Give the position of every Plasmodium parasite visible.
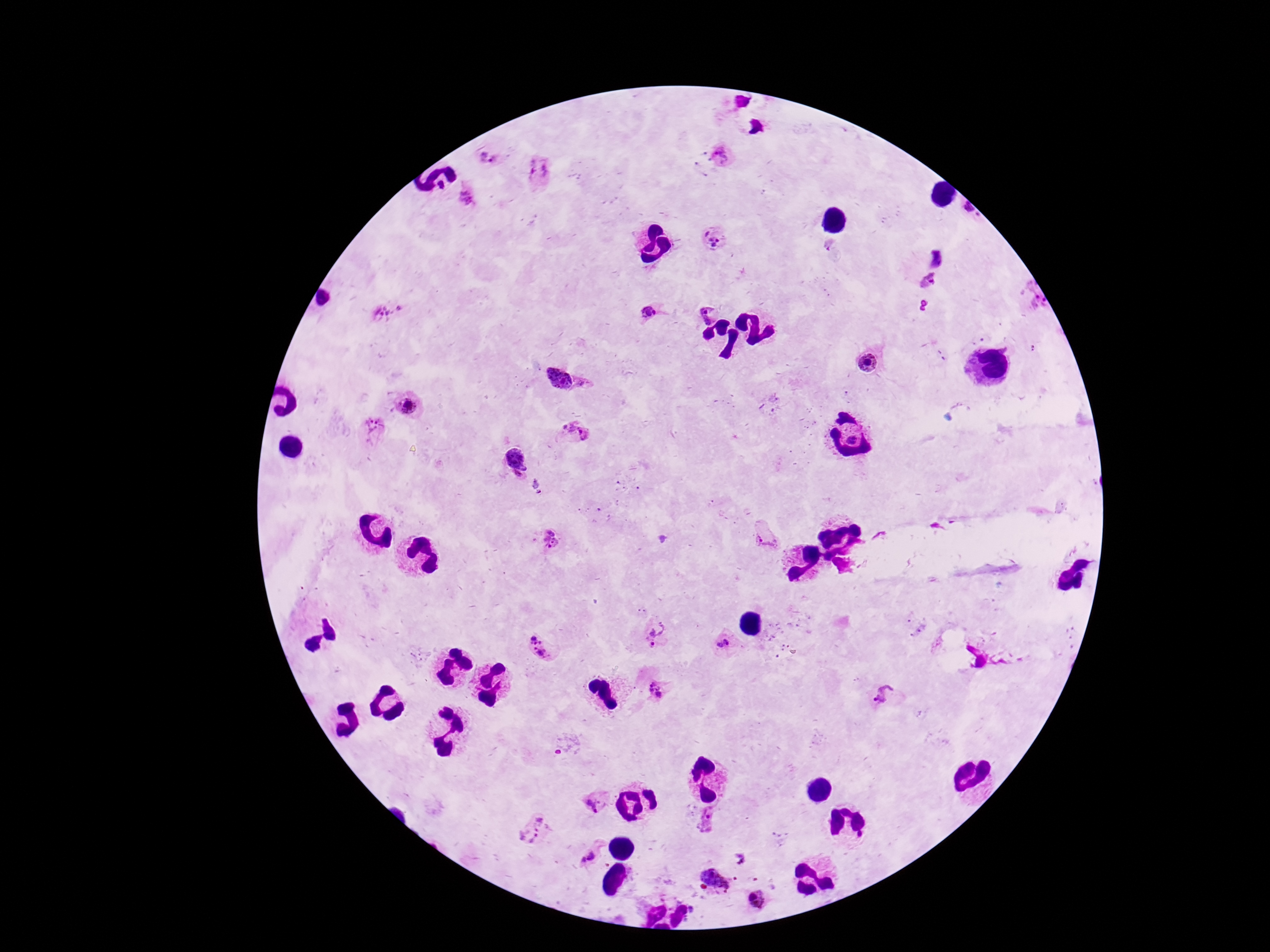
Approximate centers as {x, y} in pixels.
Plasmodium parasites: {489, 156}, {719, 158}, {537, 172}, {465, 196}, {713, 238}, {936, 256}, {929, 282}, {1028, 297}, {706, 311}, {387, 312}, {647, 314}, {868, 363}, {558, 377}, {584, 386}, {409, 404}, {372, 430}, {572, 432}, {514, 458}, {765, 536}, {551, 539}, {655, 633}, {724, 644}, {540, 648}, {658, 690}, {883, 695}, {597, 802}, {707, 818}, {533, 830}, {592, 855}, {719, 876}, {757, 900}.

{
  "preparation": "thick peripheral-blood smear",
  "magnification": "100x",
  "capture": "smartphone camera through the microscope eyepiece",
  "image_size": "1270×952 pixels",
  "stain": "Giemsa",
  "field_of_view": "one from this slide",
  "patient_malaria_status": "positive"
}